Identify the blood parasite species.
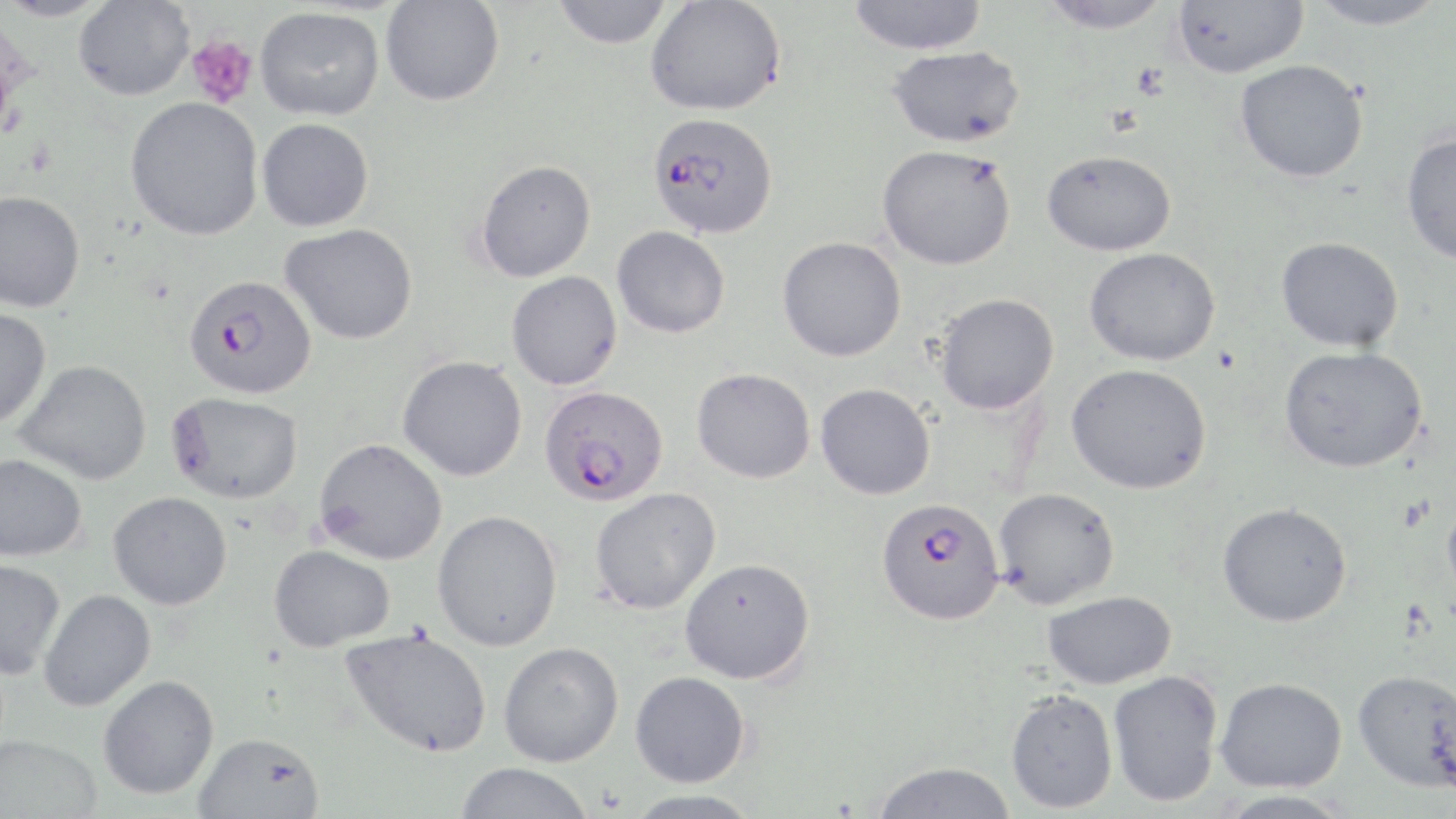

Plasmodium falciparum.

{
  "image_size": "1456×819 pixels",
  "modality": "optical microscopy",
  "plasmodium_falciparum_infected_red_blood_cell_locations": "approximate bounding boxes as named x1/y1/x2/y2 corners in pixels: (x1=648, y1=112, x2=778, y2=238), (x1=184, y1=274, x2=318, y2=400), (x1=539, y1=384, x2=669, y2=506), (x1=875, y1=497, x2=1004, y2=624)",
  "stain": "May-Grünwald-Giemsa",
  "magnification": "1000x",
  "uninfected_red_blood_cell_locations": "approximate bounding boxes as named x1/y1/x2/y2 corners in pixels: (x1=0, y1=0, x2=113, y2=21), (x1=552, y1=0, x2=674, y2=49), (x1=645, y1=0, x2=786, y2=116), (x1=846, y1=0, x2=988, y2=55), (x1=1037, y1=0, x2=1174, y2=33), (x1=1173, y1=0, x2=1308, y2=79), (x1=73, y1=1, x2=195, y2=101), (x1=381, y1=1, x2=504, y2=106), (x1=1303, y1=1, x2=1451, y2=31), (x1=255, y1=7, x2=384, y2=121), (x1=888, y1=46, x2=1026, y2=148), (x1=1235, y1=59, x2=1369, y2=183), (x1=125, y1=96, x2=264, y2=240), (x1=257, y1=118, x2=374, y2=232), (x1=1401, y1=131, x2=1456, y2=264), (x1=877, y1=144, x2=1017, y2=270), (x1=1042, y1=149, x2=1177, y2=256), (x1=476, y1=159, x2=596, y2=282), (x1=0, y1=190, x2=85, y2=312), (x1=281, y1=223, x2=418, y2=344), (x1=612, y1=226, x2=731, y2=338), (x1=777, y1=236, x2=907, y2=362), (x1=1276, y1=236, x2=1404, y2=352), (x1=1084, y1=247, x2=1222, y2=366), (x1=506, y1=271, x2=622, y2=390), (x1=934, y1=292, x2=1059, y2=414), (x1=0, y1=307, x2=51, y2=428), (x1=1279, y1=345, x2=1428, y2=473), (x1=397, y1=356, x2=528, y2=481), (x1=14, y1=359, x2=152, y2=485), (x1=1066, y1=363, x2=1212, y2=494), (x1=692, y1=367, x2=816, y2=484), (x1=815, y1=383, x2=936, y2=500), (x1=166, y1=391, x2=304, y2=504), (x1=313, y1=438, x2=448, y2=565), (x1=0, y1=453, x2=87, y2=562), (x1=590, y1=487, x2=721, y2=614), (x1=993, y1=487, x2=1120, y2=609), (x1=108, y1=491, x2=233, y2=609), (x1=1442, y1=492, x2=1456, y2=606), (x1=1218, y1=502, x2=1352, y2=627), (x1=432, y1=509, x2=563, y2=651), (x1=268, y1=544, x2=395, y2=652), (x1=680, y1=558, x2=815, y2=684), (x1=0, y1=559, x2=65, y2=680), (x1=39, y1=589, x2=156, y2=711), (x1=1042, y1=590, x2=1177, y2=689), (x1=339, y1=627, x2=492, y2=758), (x1=498, y1=641, x2=624, y2=767), (x1=1108, y1=669, x2=1224, y2=807), (x1=1353, y1=669, x2=1456, y2=792), (x1=630, y1=671, x2=751, y2=787), (x1=97, y1=675, x2=219, y2=799), (x1=1215, y1=676, x2=1347, y2=792), (x1=1006, y1=688, x2=1119, y2=814), (x1=193, y1=731, x2=325, y2=819), (x1=1, y1=735, x2=102, y2=819), (x1=870, y1=760, x2=1016, y2=819), (x1=454, y1=763, x2=594, y2=819), (x1=622, y1=789, x2=762, y2=819), (x1=1213, y1=789, x2=1355, y2=819)",
  "field_of_view": "single",
  "preparation": "thin blood smear",
  "platelet_locations": "approximate bounding boxes as named x1/y1/x2/y2 corners in pixels: (x1=186, y1=34, x2=258, y2=109), (x1=1398, y1=495, x2=1436, y2=533)"
}